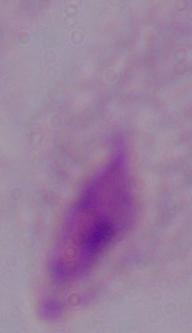

modality = micrograph
identification = trichomonad
magnification = 1000x